Name the blood parasite species.
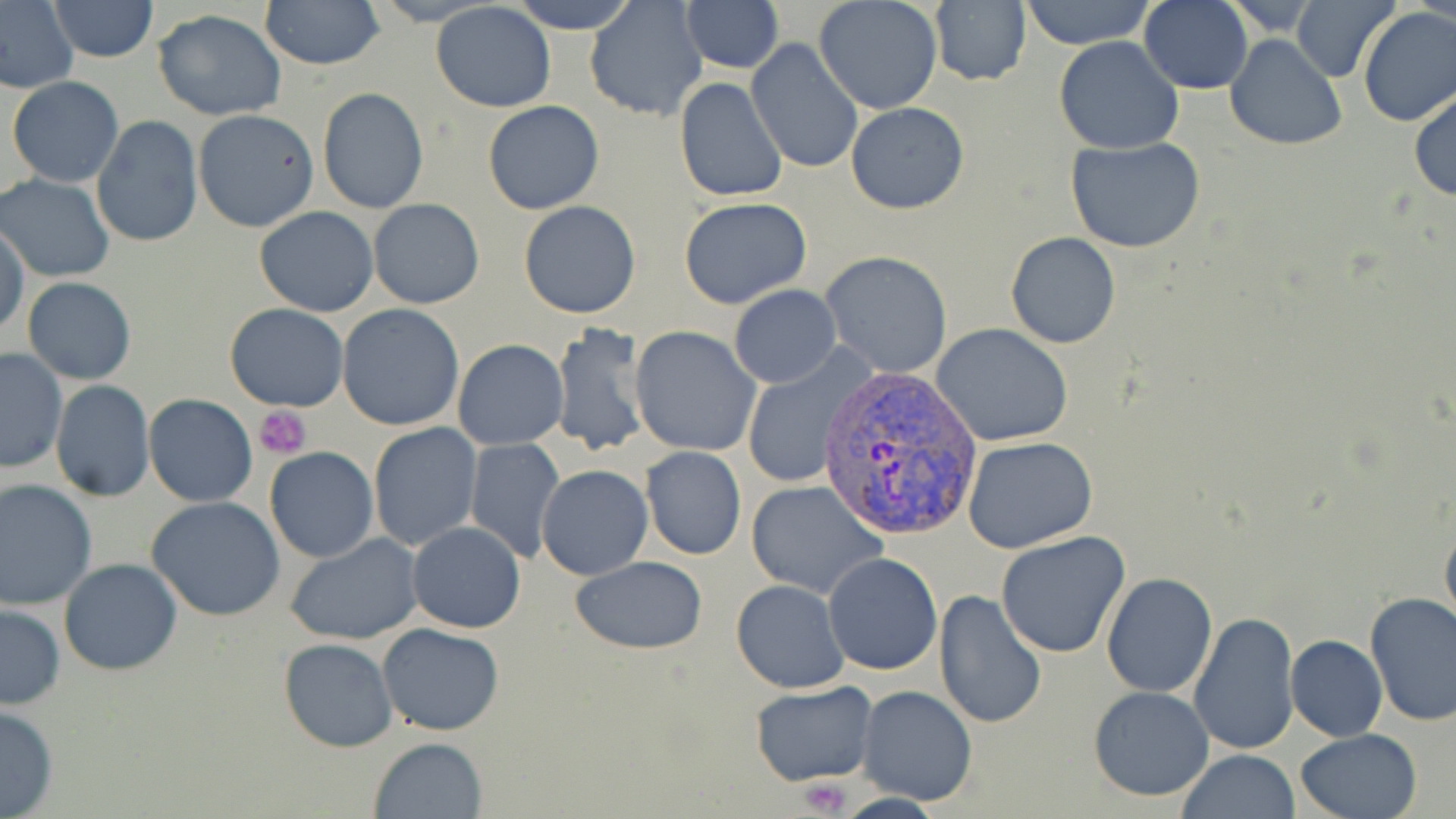

Plasmodium vivax.

magnification = 1000x
field of view = single
image size = 1456×819 pixels
modality = light microscopy
preparation = thin blood smear
Plasmodium vivax-infected red blood cell locations = approximate bounding boxes as [x1, y1, x2, y2] in pixels: [817, 366, 977, 539]
uninfected red blood cell locations = approximate bounding boxes as [x1, y1, x2, y2] in pixels: [0, 0, 79, 94], [47, 0, 160, 62], [261, 0, 385, 71], [507, 0, 640, 34], [583, 0, 710, 120], [680, 0, 784, 73], [930, 0, 1030, 89], [1018, 0, 1155, 49], [1139, 0, 1254, 94], [1293, 0, 1400, 82], [813, 1, 943, 114], [431, 3, 556, 113], [152, 8, 286, 121], [1357, 8, 1456, 128], [1225, 34, 1346, 152], [1053, 36, 1185, 154], [748, 38, 864, 175], [7, 76, 124, 187], [676, 76, 789, 202], [318, 87, 429, 212], [1410, 89, 1456, 201], [482, 100, 606, 216], [845, 101, 970, 215], [193, 109, 320, 233], [92, 114, 204, 250], [1064, 137, 1210, 255], [1, 174, 115, 282], [368, 198, 484, 310], [679, 198, 813, 311], [517, 201, 642, 319], [255, 206, 379, 316], [1, 220, 27, 336], [1005, 233, 1121, 349], [820, 252, 952, 377], [23, 276, 136, 384], [729, 286, 840, 387], [224, 304, 349, 412], [336, 304, 466, 432], [549, 323, 651, 458], [932, 323, 1073, 448], [629, 327, 762, 456], [453, 339, 568, 451], [0, 347, 69, 474], [740, 349, 873, 491], [50, 380, 155, 502], [145, 394, 256, 507], [368, 423, 483, 551], [962, 435, 1098, 553], [465, 438, 565, 562], [640, 446, 746, 560], [265, 447, 379, 563], [536, 465, 653, 581], [0, 478, 98, 607], [746, 480, 889, 600], [147, 496, 286, 622], [1439, 513, 1456, 636], [408, 522, 526, 633], [993, 531, 1133, 659], [284, 533, 424, 643], [823, 553, 942, 675], [571, 556, 707, 655], [59, 559, 183, 676], [1101, 572, 1217, 697], [731, 579, 849, 692], [934, 588, 1047, 729], [1364, 591, 1456, 727], [1, 603, 65, 709], [1188, 609, 1300, 755], [377, 623, 505, 735], [1285, 635, 1387, 741], [280, 637, 397, 751], [751, 681, 875, 786], [856, 685, 979, 807], [1088, 686, 1215, 801], [0, 703, 59, 817], [1295, 729, 1423, 819], [370, 737, 488, 818], [1177, 749, 1299, 819]
platelet locations = approximate bounding boxes as [x1, y1, x2, y2] in pixels: [253, 406, 312, 459], [797, 777, 852, 815]
stain = May-Grünwald-Giemsa